Identify the parasite.
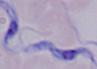
This is a trypanosome.

Photomicrograph. 1000x magnification.